Locate every uninfected red blood cell.
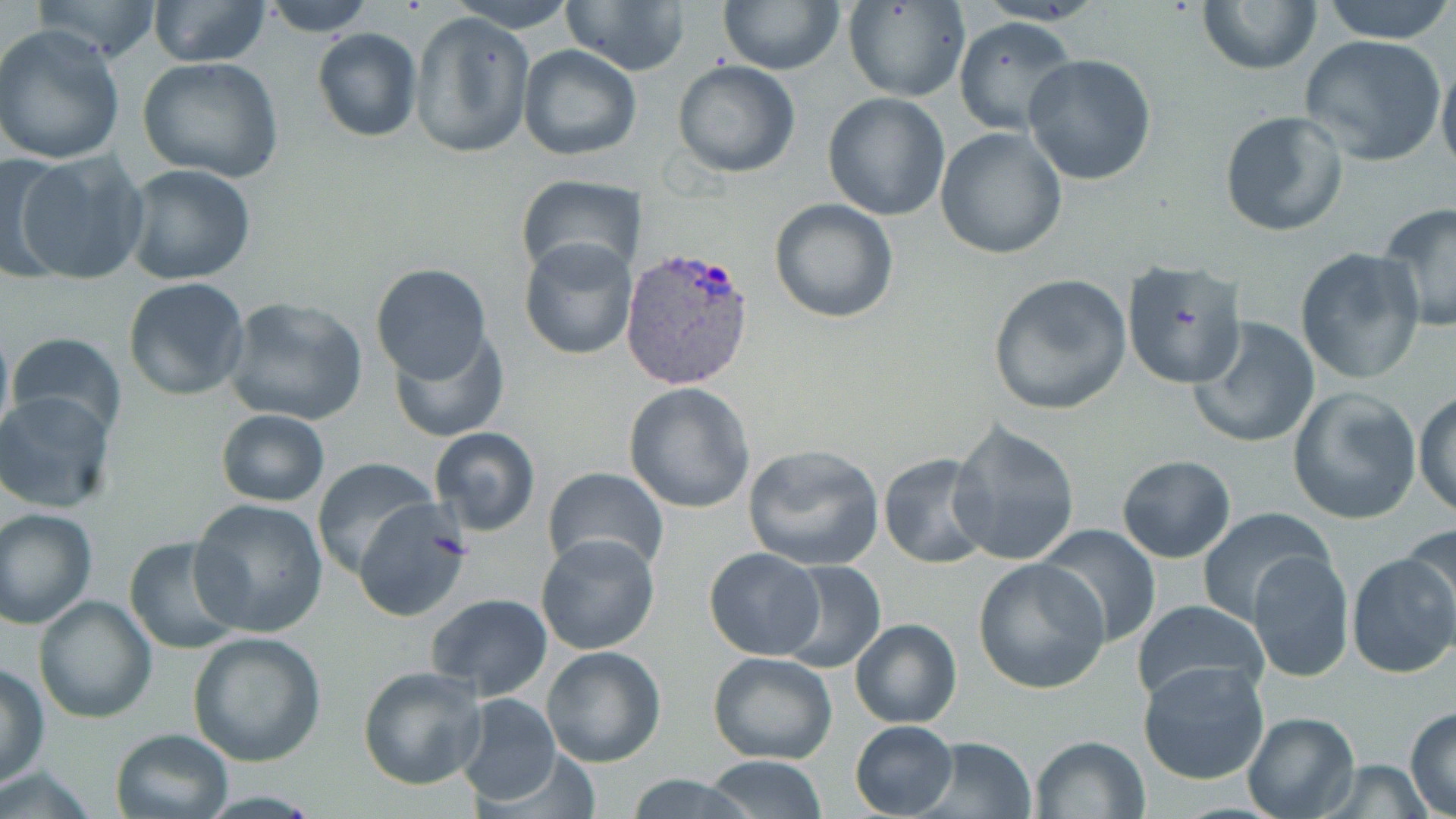

Approximate bounding boxes as (x1, y1, x2, y2) in pixels.
Uninfected red blood cells: (30, 0, 162, 64), (149, 0, 273, 67), (257, 0, 378, 35), (445, 0, 580, 31), (561, 0, 692, 77), (842, 0, 969, 103), (718, 1, 845, 76), (1197, 1, 1322, 76), (1320, 1, 1456, 44), (407, 12, 534, 158), (953, 16, 1078, 136), (0, 25, 125, 165), (311, 27, 423, 142), (1299, 35, 1444, 166), (518, 44, 641, 161), (1436, 51, 1456, 182), (1023, 54, 1157, 186), (137, 56, 284, 183), (672, 60, 801, 178), (822, 92, 951, 221), (1220, 110, 1349, 237), (936, 127, 1066, 259), (12, 151, 150, 286), (1, 152, 69, 282), (122, 163, 258, 285), (516, 176, 646, 278), (768, 197, 899, 324), (1378, 202, 1456, 331), (518, 239, 636, 359), (1295, 248, 1425, 385), (1119, 261, 1251, 392), (370, 263, 491, 381), (987, 274, 1133, 416), (122, 277, 250, 401), (220, 296, 369, 426), (1189, 314, 1320, 450), (0, 319, 14, 453), (386, 327, 510, 443), (8, 333, 127, 442), (623, 383, 755, 514), (1286, 386, 1421, 525), (1414, 390, 1456, 519), (0, 393, 119, 516), (216, 409, 330, 507), (947, 420, 1082, 566), (429, 427, 541, 534), (742, 444, 887, 571), (878, 454, 996, 569), (1118, 455, 1235, 563), (310, 457, 436, 576), (542, 466, 670, 575), (190, 498, 330, 636), (352, 500, 474, 624), (0, 508, 97, 628), (1193, 509, 1330, 624), (1038, 523, 1160, 647), (1401, 523, 1455, 650), (538, 534, 660, 656), (123, 536, 246, 655), (703, 547, 825, 661), (1247, 550, 1354, 681), (1344, 552, 1456, 680), (973, 558, 1110, 695), (775, 560, 887, 674), (427, 593, 553, 701), (34, 595, 157, 724), (1130, 599, 1271, 710), (849, 617, 963, 728), (187, 630, 327, 767), (541, 645, 667, 768), (708, 651, 838, 765), (1138, 659, 1271, 786), (359, 663, 487, 790), (0, 664, 50, 788), (454, 693, 560, 806), (1404, 707, 1456, 818), (1242, 711, 1360, 819), (849, 720, 959, 818), (109, 728, 232, 818), (1029, 734, 1149, 818), (913, 735, 1038, 818), (700, 755, 830, 819), (1314, 760, 1431, 818), (1, 763, 100, 818), (627, 774, 748, 818).

Plasmodium vivax-infected red blood cell locations: (621, 244, 756, 391). Slide-level diagnosis: Plasmodium vivax. Image is 1456×819 pixels. May-Grünwald-Giemsa-stained preparation. Single field of view. Thin blood smear. 1000x magnification. Optical microscopy.